Describe the morphology of the erythrocytes.
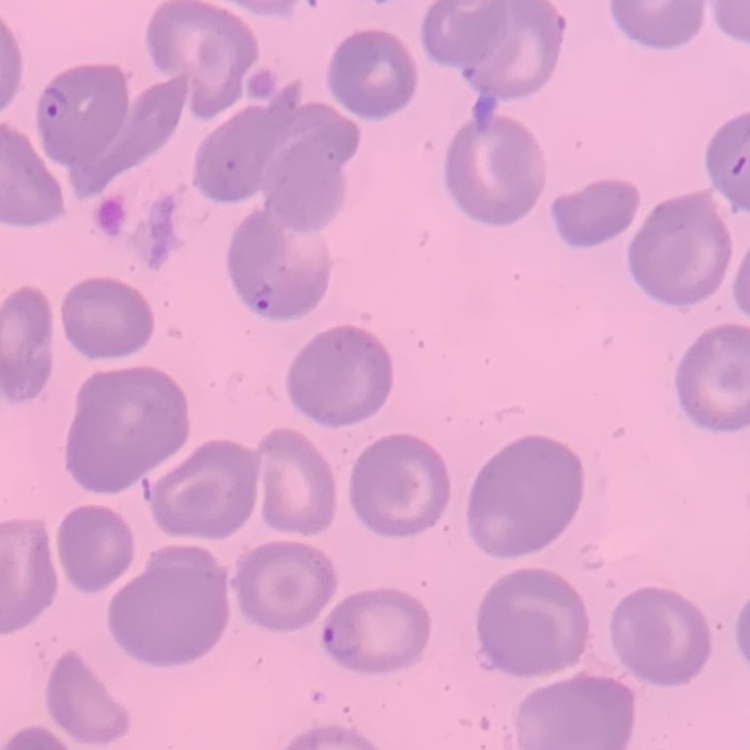
No rouleaux formation.

Field's or Giemsa stain. One tile cut from a larger photomicrograph. Thin blood film.